Assess the morphology of the red blood cells.
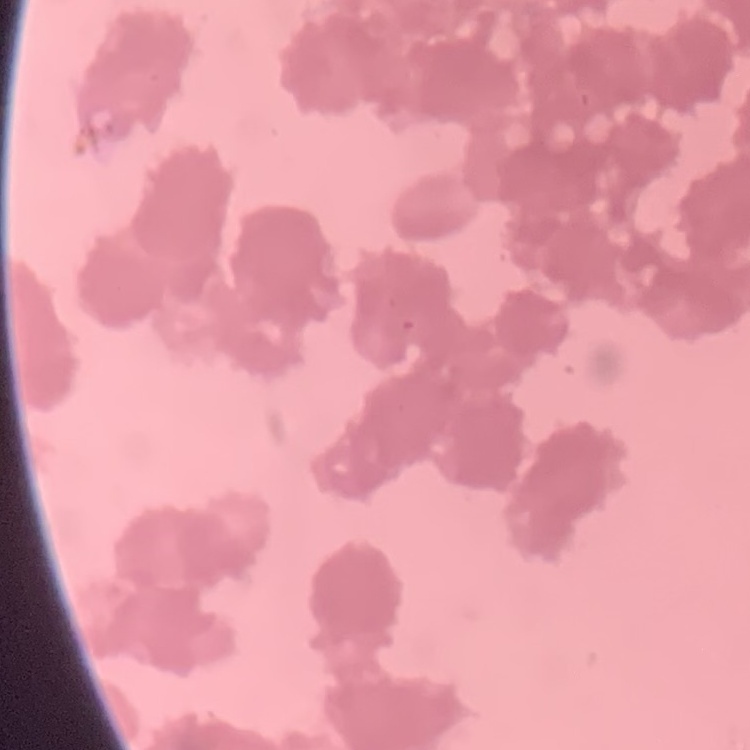

Rouleaux formation.

stain = Field's or Giemsa
preparation = thin blood smear
image type = one tile cut from a larger photomicrograph